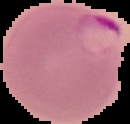
Image is 130×124 pixels. Result: Plasmodium parasites identified. Segmented cell region on a black background. From a thin blood smear.